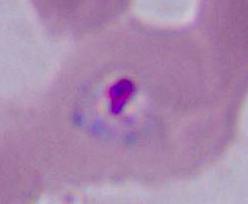

identification: Plasmodium
modality: micrograph
magnification: 400x or 1000x